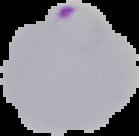

image type = segmented cell region with the area outside set to black
preparation = thin blood smear
result = malaria parasites detected
image size = 139×136 pixels